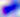 Micrograph. Toxoplasma gondii is shown. Captured at 400x magnification.